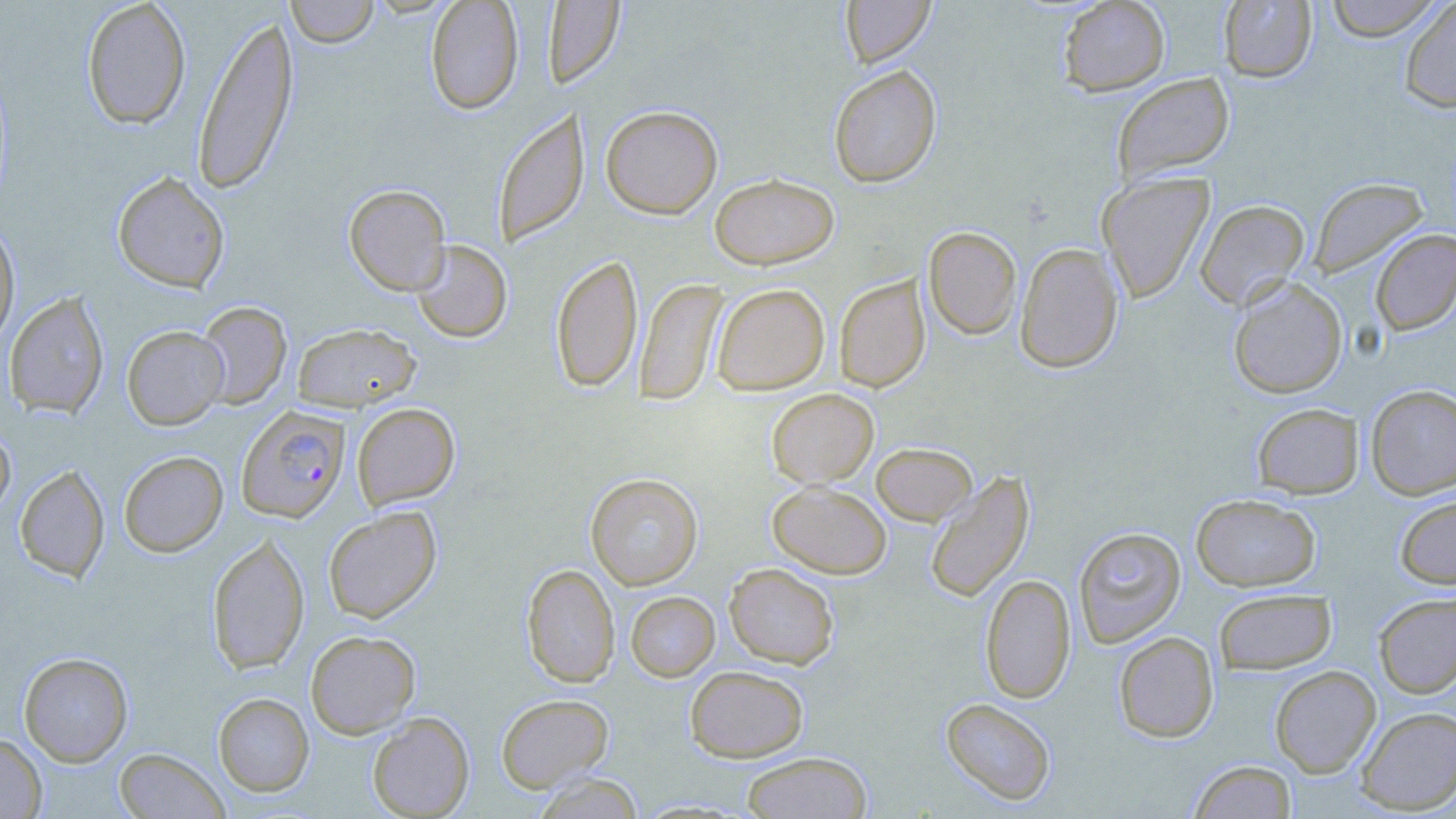
slide-level diagnosis = Plasmodium falciparum
magnification = 1000x
stain = May-Grünwald-Giemsa
image size = 1456×819 pixels
modality = light microscopy
field of view = one of a larger specimen
Plasmodium falciparum-infected red blood cell locations = approximate bounding boxes as (x1,y1)-(x2,y2) corner pairs in pixels: (237,406)-(351,523)
uninfected red blood cell locations = approximate bounding boxes as (x1,y1)-(x2,y2) corner pairs in pixels: (81,0)-(192,130), (285,0)-(380,47), (425,0)-(524,115), (840,0)-(935,68), (1057,0)-(1170,96), (1324,0)-(1445,41), (544,1)-(625,87), (1218,1)-(1317,82), (1399,1)-(1456,113), (193,13)-(299,195), (828,65)-(942,187), (1111,72)-(1235,185), (600,105)-(723,218), (493,106)-(589,248), (112,171)-(230,293), (1097,172)-(1215,303), (709,173)-(839,269), (1307,177)-(1429,279), (344,184)-(451,295), (1195,199)-(1310,310), (0,218)-(20,349), (923,226)-(1022,339), (1370,229)-(1456,336), (410,239)-(512,343), (1015,242)-(1124,373), (551,254)-(643,393), (835,275)-(930,392), (1227,277)-(1348,399), (634,278)-(727,405), (711,283)-(830,395), (3,291)-(110,419), (194,301)-(292,410), (292,322)-(421,411), (121,325)-(229,429), (1365,383)-(1456,499), (766,388)-(879,488), (1251,402)-(1363,498), (351,403)-(460,509), (0,426)-(15,521), (871,442)-(977,525), (119,451)-(228,557), (15,464)-(110,582), (924,470)-(1035,604), (585,473)-(703,590), (767,481)-(892,578), (1191,493)-(1321,592), (1394,494)-(1456,589), (323,506)-(442,623), (1073,526)-(1186,647), (207,533)-(310,675), (521,563)-(620,688), (725,563)-(839,668), (980,574)-(1076,703), (1214,587)-(1337,674), (625,591)-(720,682), (1373,592)-(1456,699), (305,630)-(420,738), (1114,631)-(1219,742), (18,651)-(133,766), (684,665)-(808,762), (1270,665)-(1381,778), (213,692)-(314,796), (496,693)-(613,792), (940,698)-(1057,806), (1355,706)-(1456,814), (367,712)-(475,818), (0,733)-(47,818), (114,748)-(229,819), (740,752)-(872,818), (1188,760)-(1297,818), (532,773)-(645,819)
preparation = thin blood film